State which parasite is depicted.
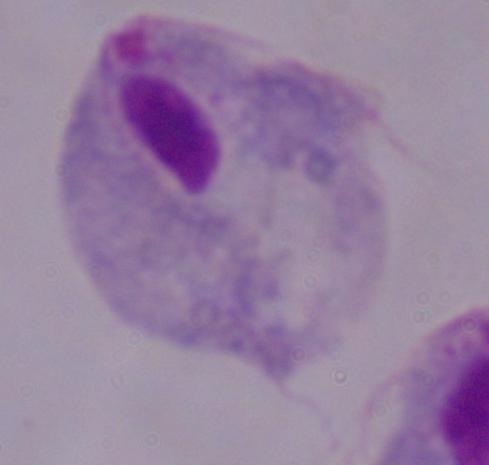

A trichomonad.

Photomicrograph. 1000x magnification.